Classify this cell by malaria status.
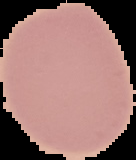

It is uninfected.

Segmented cell region on a black background. From a thin blood film. Image is 136×160 pixels.